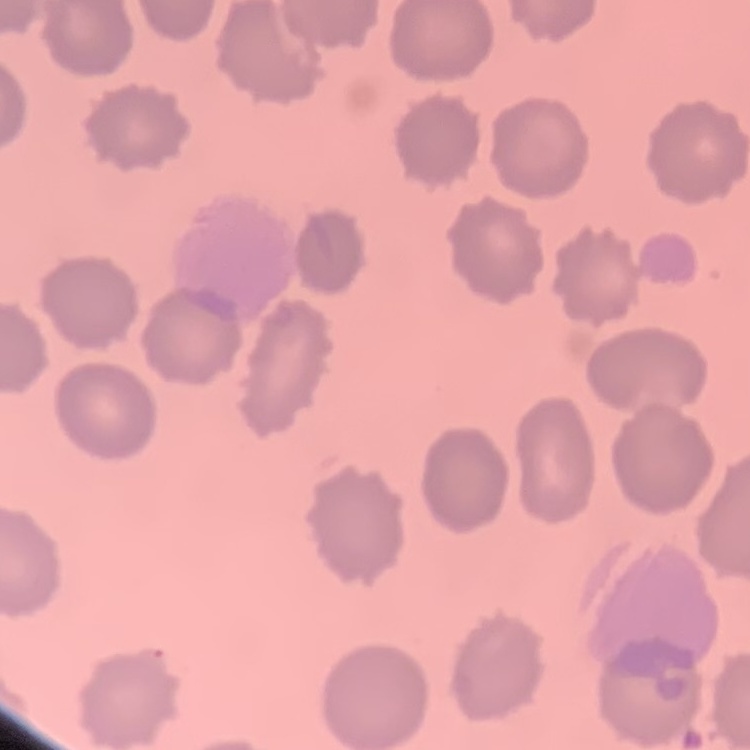

Summary:
  - Red blood cell morphology: no rouleaux formation
  - Preparation: thin peripheral smear
  - Stain: Field's or Giemsa
  - Image type: one tile cut from a larger photomicrograph